Classify this cell by malaria status.
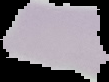
Uninfected.

Summary:
  - Preparation: thin blood film
  - Image size: 109×82 pixels
  - Image type: segmented cell region with the area outside set to black